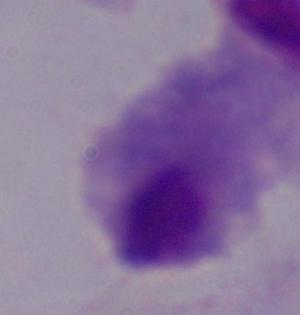
identification: trichomonad
modality: photomicrograph
magnification: 1000x